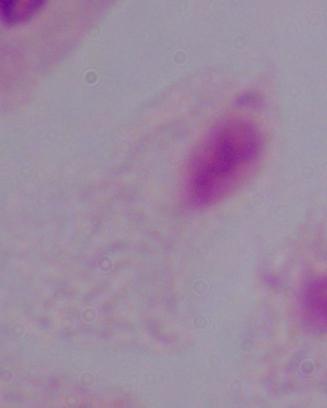

Summary:
  - Magnification: 1000x
  - Modality: micrograph
  - Identification: trichomonad